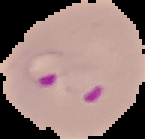

Image is 145×139 pixels. Result: Plasmodium parasites detected. The area outside the segmented cell region is set to black. From a thin blood film.